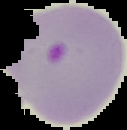
preparation: thin blood film
result: malaria parasites detected
image_type: cell region segmented out of the field of view; surrounding area masked to black
image_size: 127×130 pixels